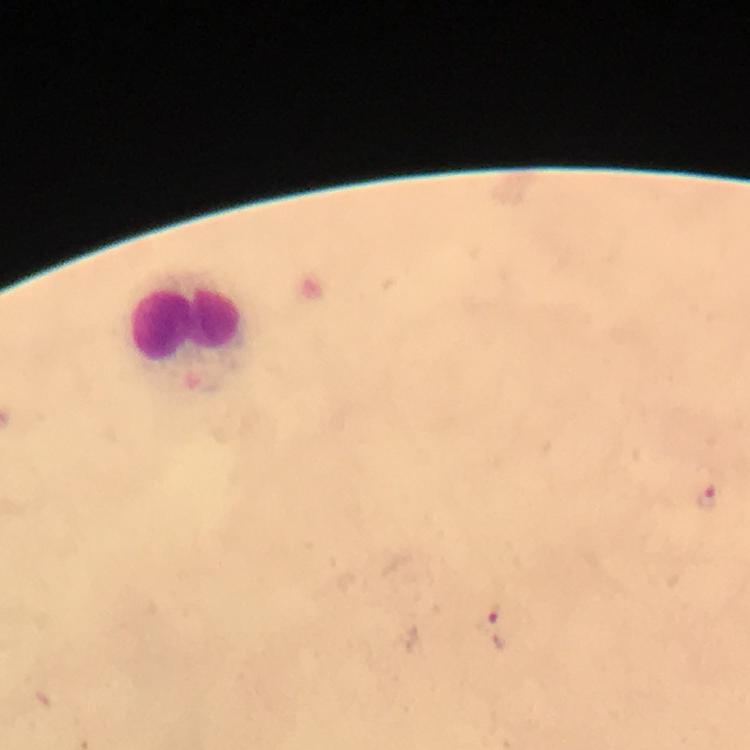
leukocyte locations = approximate centers as (x, y) in pixels: (188, 324)
Plasmodium parasite locations = approximate centers as (x, y) in pixels: (708, 497), (495, 626)
context = from a malaria diagnostic workup
image size = 750×750 pixels
capture = smartphone camera through the microscope
immersion oil = applied
magnification = 100x
stain = Giemsa
preparation = thick smear
cropped from = one field of view